Point out each Plasmodium parasite and each leukocyte.
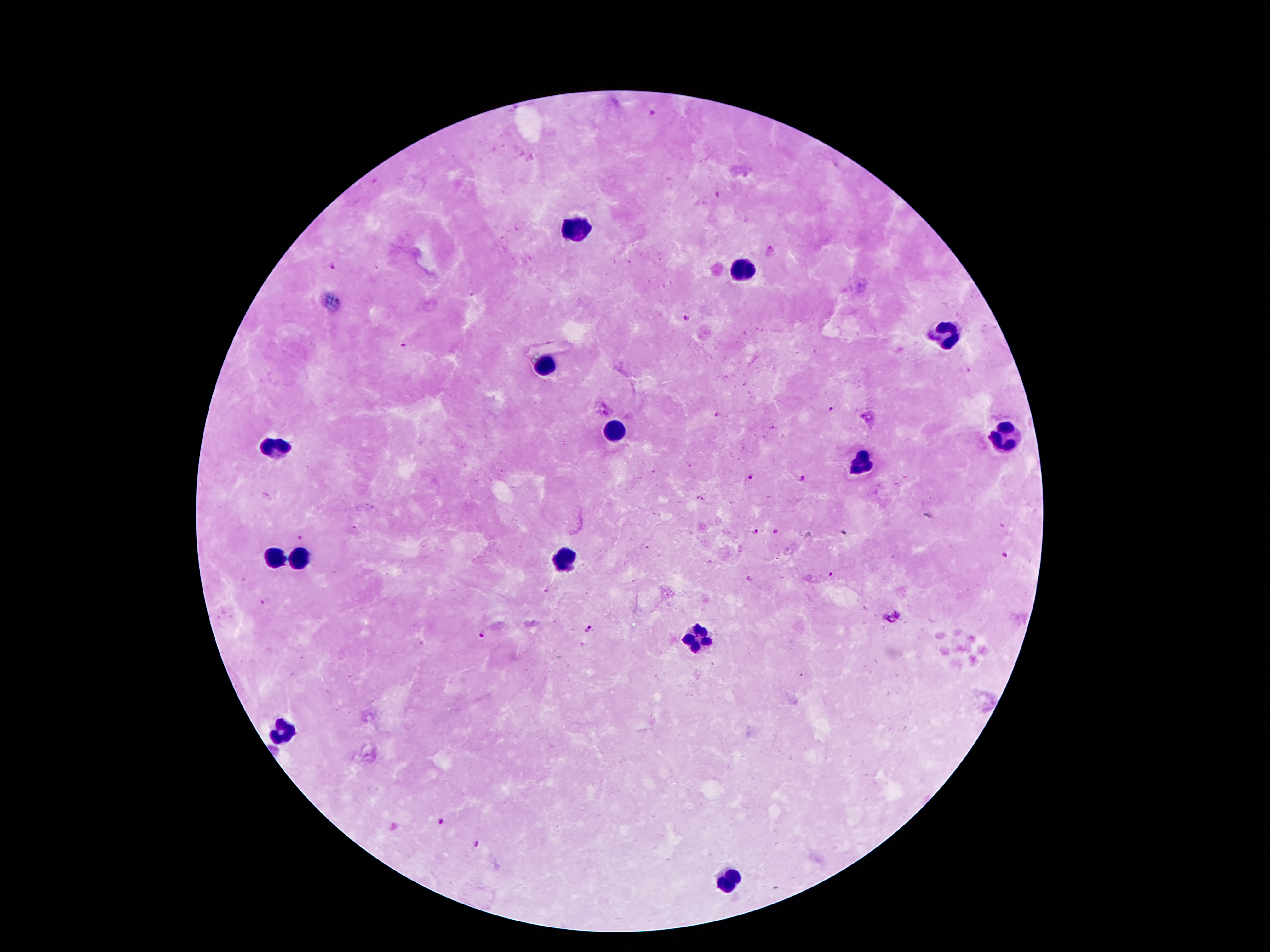
Approximate centers as [x, y] in pixels.
Plasmodium parasites: [651, 114], [335, 268], [688, 320], [402, 343], [830, 411], [605, 412], [749, 477], [801, 478], [755, 531], [1005, 556], [830, 573], [750, 579], [262, 602], [589, 630], [480, 637], [439, 821], [477, 844].
Leukocytes: [577, 230], [745, 268], [947, 337], [546, 365], [615, 428], [1008, 436], [275, 449], [859, 459], [304, 556], [565, 558], [273, 560], [697, 638], [288, 730], [731, 879].

Patient malaria status: infected with Plasmodium falciparum. 100x magnification. Thick blood film. One field from this slide. Image is 1270×952 pixels. Photographed through the microscope eyepiece with a smartphone camera. Giemsa-stained preparation.